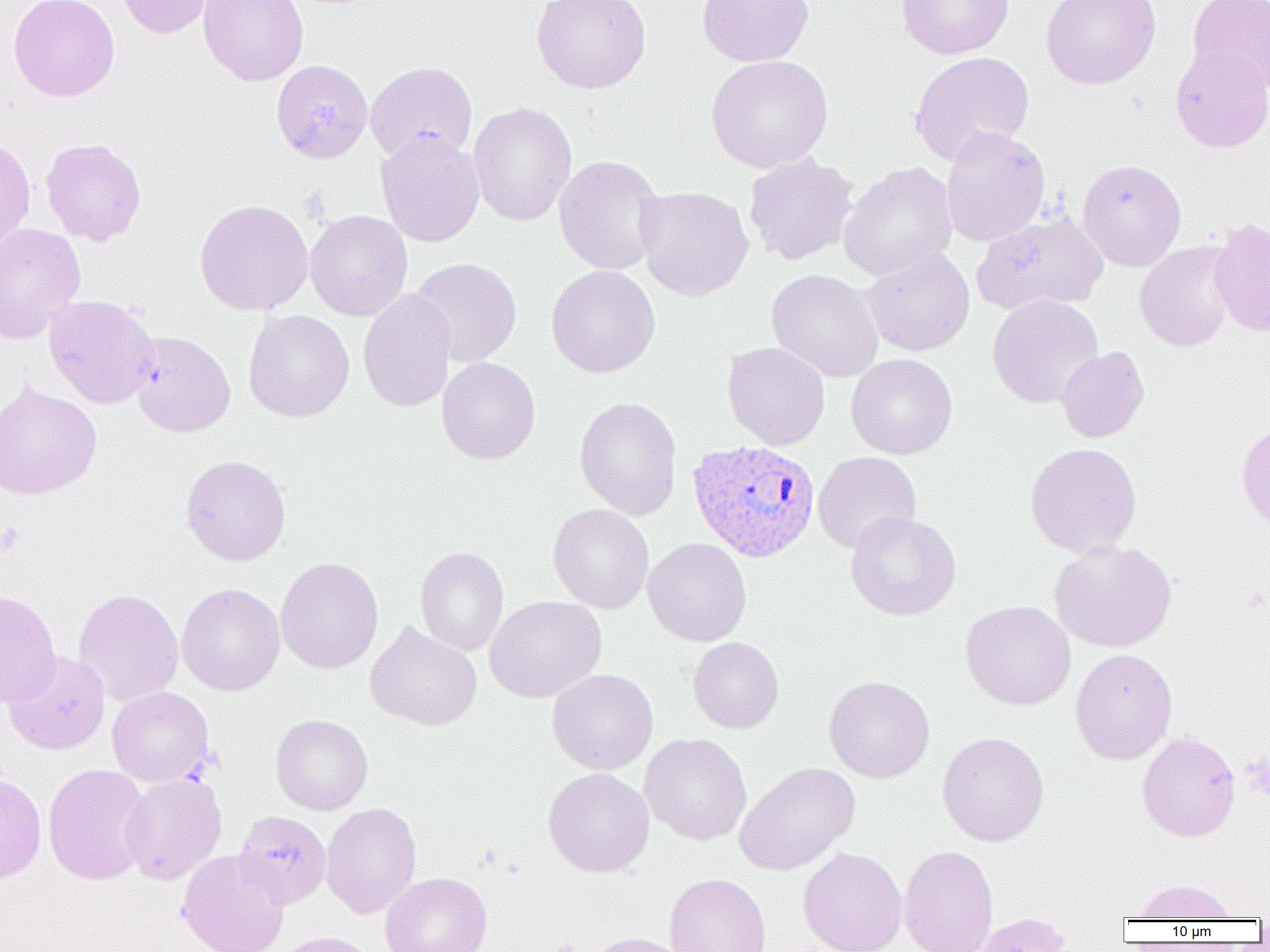
Approximate bounding boxes as (x1,y1)-(x2,y2) corner pairs in pixels. Uninfected red blood cell locations: (8,0)-(120,102), (116,0)-(215,38), (198,0)-(309,87), (531,0)-(651,94), (696,0)-(814,67), (896,0)-(1014,60), (1041,0)-(1161,89), (1186,0)-(1270,94), (1170,44)-(1270,152), (909,51)-(1035,165), (706,55)-(833,173), (271,59)-(373,164), (365,61)-(478,164), (468,102)-(577,226), (940,126)-(1051,247), (375,130)-(485,247), (0,136)-(35,254), (41,137)-(146,246), (743,153)-(857,265), (553,155)-(667,275), (1077,158)-(1186,270), (838,162)-(958,282), (635,186)-(754,301), (193,199)-(314,315), (305,210)-(413,321), (971,211)-(1108,315), (1209,218)-(1270,336), (0,221)-(86,343), (1135,240)-(1237,352), (860,247)-(976,357), (411,257)-(522,367), (546,265)-(660,378), (766,268)-(883,382), (357,289)-(456,412), (44,294)-(160,409), (987,294)-(1103,408), (243,309)-(355,422), (129,331)-(235,437), (722,341)-(830,450), (1056,346)-(1150,443), (846,354)-(958,459), (437,357)-(540,465), (0,381)-(101,500), (574,396)-(682,520), (1236,418)-(1270,533), (1024,442)-(1142,558), (813,451)-(921,554), (181,454)-(291,566), (547,503)-(654,613), (845,510)-(962,621), (644,537)-(751,646), (1049,540)-(1177,653), (415,546)-(508,656), (275,556)-(383,674), (177,583)-(285,695), (73,588)-(183,706), (0,589)-(61,708), (485,596)-(606,703), (961,600)-(1076,710), (365,621)-(482,731), (687,637)-(784,734), (1071,648)-(1177,764), (3,650)-(110,755), (547,669)-(658,775), (824,675)-(935,782), (107,686)-(214,787), (271,714)-(373,815), (937,731)-(1049,846), (1137,731)-(1240,842), (640,733)-(752,845), (734,762)-(860,875), (42,763)-(154,885), (543,768)-(654,877), (0,772)-(47,883), (120,773)-(227,884), (321,803)-(422,918), (231,811)-(331,910), (899,844)-(999,952), (797,847)-(907,952), (176,849)-(289,952), (380,872)-(492,952), (664,873)-(772,952), (1132,878)-(1241,920), (970,912)-(1073,952), (270,931)-(384,952), (583,933)-(692,952). Plasmodium ovale-infected red blood cell locations: (687,439)-(820,563). Platelet locations: (0,520)-(25,556). Slide-level diagnosis: Plasmodium ovale. Thin blood smear. One field of a larger specimen. Image is 1270×952 pixels. Light microscopy. 1000x magnification.